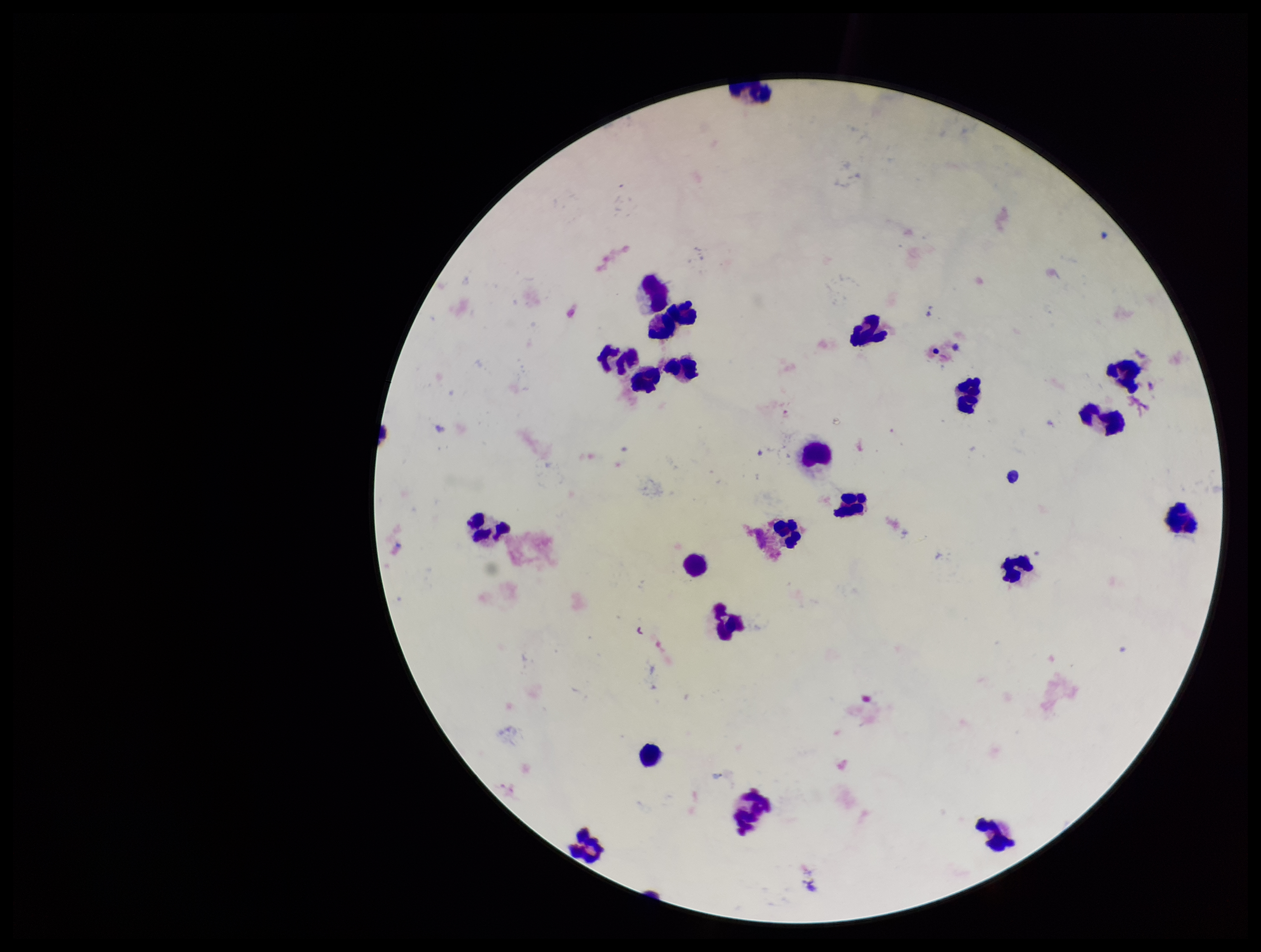
Summary:
  - Stain: Giemsa
  - Capture: smartphone photograph through the microscope eyepiece
  - Parasite count: 0
  - Plasmodium parasites: none identified
  - Patient malaria status: negative
  - Field of view: one from this slide
  - Image size: 1261×952 pixels
  - Preparation: thick
  - Leukocyte count: 22